Comment on the morphology of the erythrocytes.
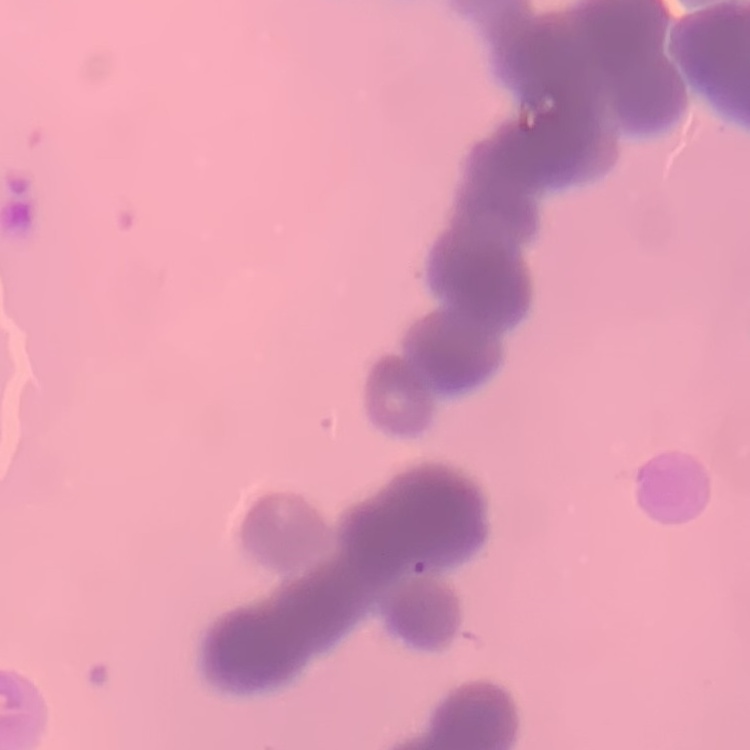

They show rouleaux formation.

Summary:
  - Preparation: thin blood film
  - Image type: one tile cut from a larger photomicrograph
  - Stain: Field's or Giemsa